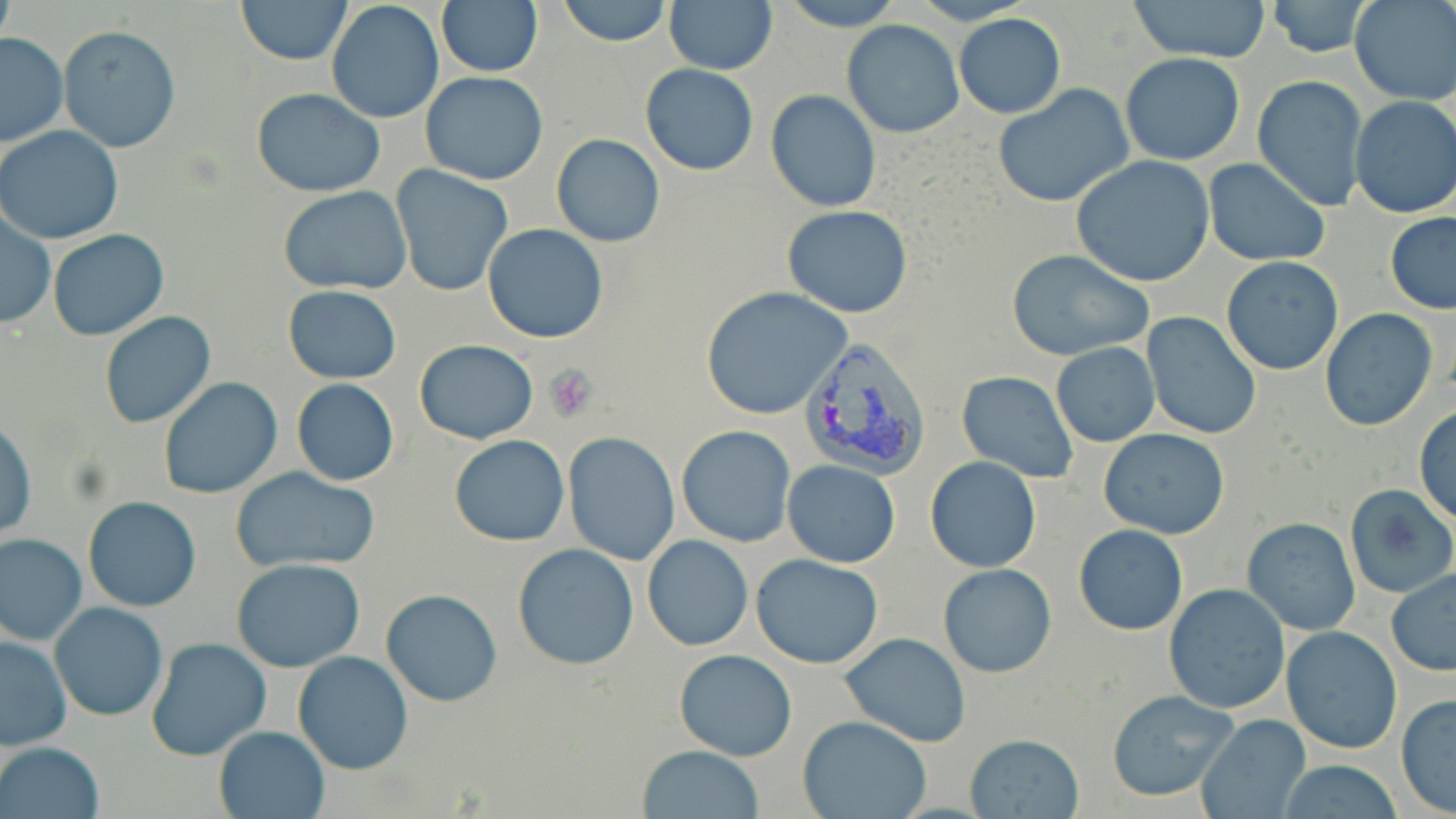

Summary:
  - Coordinate format: approximate bounding boxes as named x1/y1/x2/y2 corners in pixels
  - Platelet locations: (x1=545, y1=366, x2=598, y2=420)
  - Uninfected red blood cell locations: (x1=238, y1=0, x2=350, y2=64), (x1=557, y1=0, x2=673, y2=47), (x1=775, y1=0, x2=906, y2=31), (x1=1124, y1=0, x2=1274, y2=64), (x1=1350, y1=0, x2=1456, y2=104), (x1=665, y1=1, x2=777, y2=73), (x1=1265, y1=1, x2=1372, y2=56), (x1=0, y1=2, x2=17, y2=52), (x1=436, y1=2, x2=543, y2=76), (x1=327, y1=4, x2=442, y2=124), (x1=954, y1=13, x2=1066, y2=118), (x1=842, y1=19, x2=965, y2=137), (x1=59, y1=25, x2=180, y2=152), (x1=0, y1=34, x2=68, y2=149), (x1=1120, y1=53, x2=1246, y2=166), (x1=640, y1=65, x2=759, y2=176), (x1=419, y1=72, x2=548, y2=185), (x1=1252, y1=75, x2=1368, y2=212), (x1=993, y1=84, x2=1135, y2=208), (x1=251, y1=87, x2=385, y2=196), (x1=766, y1=91, x2=881, y2=212), (x1=1350, y1=95, x2=1456, y2=220), (x1=0, y1=125, x2=125, y2=244), (x1=551, y1=133, x2=665, y2=247), (x1=1070, y1=155, x2=1216, y2=286), (x1=1203, y1=159, x2=1330, y2=268), (x1=391, y1=165, x2=513, y2=296), (x1=280, y1=186, x2=411, y2=295), (x1=782, y1=205, x2=913, y2=317), (x1=1, y1=211, x2=55, y2=328), (x1=1385, y1=212, x2=1456, y2=312), (x1=482, y1=223, x2=608, y2=344), (x1=47, y1=229, x2=169, y2=341), (x1=1006, y1=249, x2=1155, y2=361), (x1=1221, y1=256, x2=1344, y2=375), (x1=283, y1=286, x2=401, y2=383), (x1=700, y1=287, x2=850, y2=418), (x1=1319, y1=307, x2=1438, y2=431), (x1=99, y1=312, x2=215, y2=428), (x1=1140, y1=312, x2=1262, y2=441), (x1=414, y1=339, x2=537, y2=444), (x1=1050, y1=343, x2=1160, y2=447), (x1=956, y1=371, x2=1079, y2=484), (x1=157, y1=377, x2=283, y2=499), (x1=292, y1=378, x2=399, y2=487), (x1=1414, y1=405, x2=1456, y2=526), (x1=0, y1=417, x2=36, y2=543), (x1=677, y1=425, x2=796, y2=547), (x1=1099, y1=429, x2=1229, y2=539), (x1=563, y1=432, x2=680, y2=565), (x1=448, y1=434, x2=569, y2=546), (x1=924, y1=455, x2=1041, y2=573), (x1=783, y1=459, x2=900, y2=567), (x1=230, y1=466, x2=381, y2=574), (x1=1344, y1=483, x2=1456, y2=599), (x1=82, y1=496, x2=201, y2=613), (x1=1242, y1=518, x2=1361, y2=635), (x1=1074, y1=524, x2=1187, y2=635), (x1=0, y1=534, x2=87, y2=646), (x1=642, y1=535, x2=753, y2=652), (x1=512, y1=543, x2=639, y2=668), (x1=752, y1=554, x2=884, y2=670), (x1=229, y1=558, x2=368, y2=673), (x1=939, y1=564, x2=1056, y2=678), (x1=1386, y1=569, x2=1456, y2=676), (x1=1164, y1=584, x2=1291, y2=716), (x1=380, y1=589, x2=501, y2=707), (x1=49, y1=601, x2=167, y2=722), (x1=1280, y1=627, x2=1402, y2=755), (x1=0, y1=633, x2=71, y2=749), (x1=839, y1=634, x2=971, y2=746), (x1=144, y1=637, x2=273, y2=762), (x1=674, y1=649, x2=799, y2=761), (x1=293, y1=651, x2=413, y2=773), (x1=1106, y1=689, x2=1242, y2=803), (x1=1395, y1=693, x2=1455, y2=816), (x1=1195, y1=713, x2=1311, y2=819), (x1=797, y1=715, x2=931, y2=819), (x1=213, y1=726, x2=329, y2=818), (x1=964, y1=732, x2=1086, y2=818), (x1=0, y1=741, x2=105, y2=819), (x1=637, y1=745, x2=765, y2=818), (x1=1274, y1=760, x2=1407, y2=818)
  - Plasmodium vivax-infected red blood cell locations: (x1=799, y1=337, x2=932, y2=481)
  - Slide-level diagnosis: Plasmodium vivax
  - Preparation: thin blood film
  - Field of view: single
  - Magnification: 1000x
  - Modality: optical microscopy
  - Image size: 1456×819 pixels
  - Stain: May-Grünwald-Giemsa